Describe the morphology of the red blood cells.
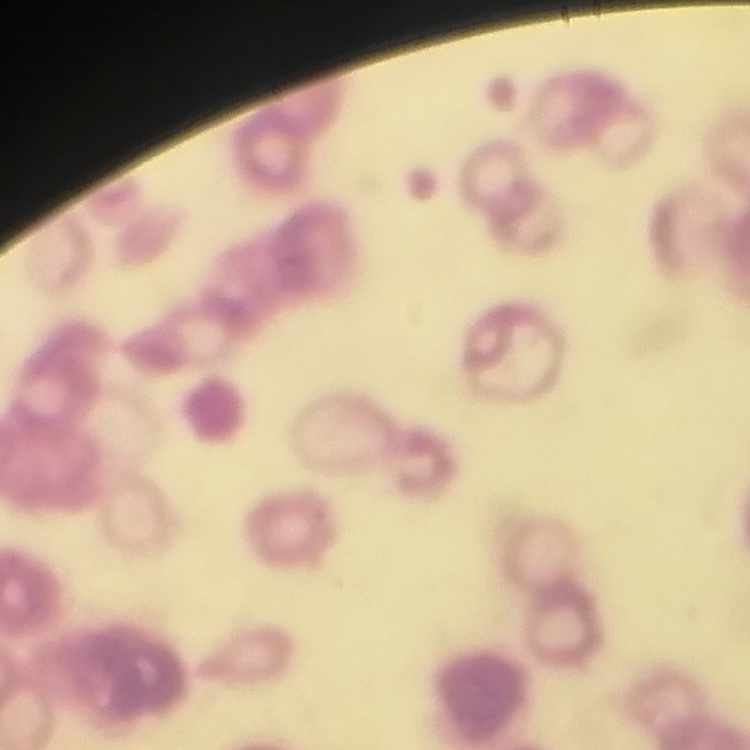
Rouleaux formation.

Summary:
  - Image type: one tile cut from a larger photomicrograph
  - Stain: Field's or Giemsa
  - Preparation: thin blood film